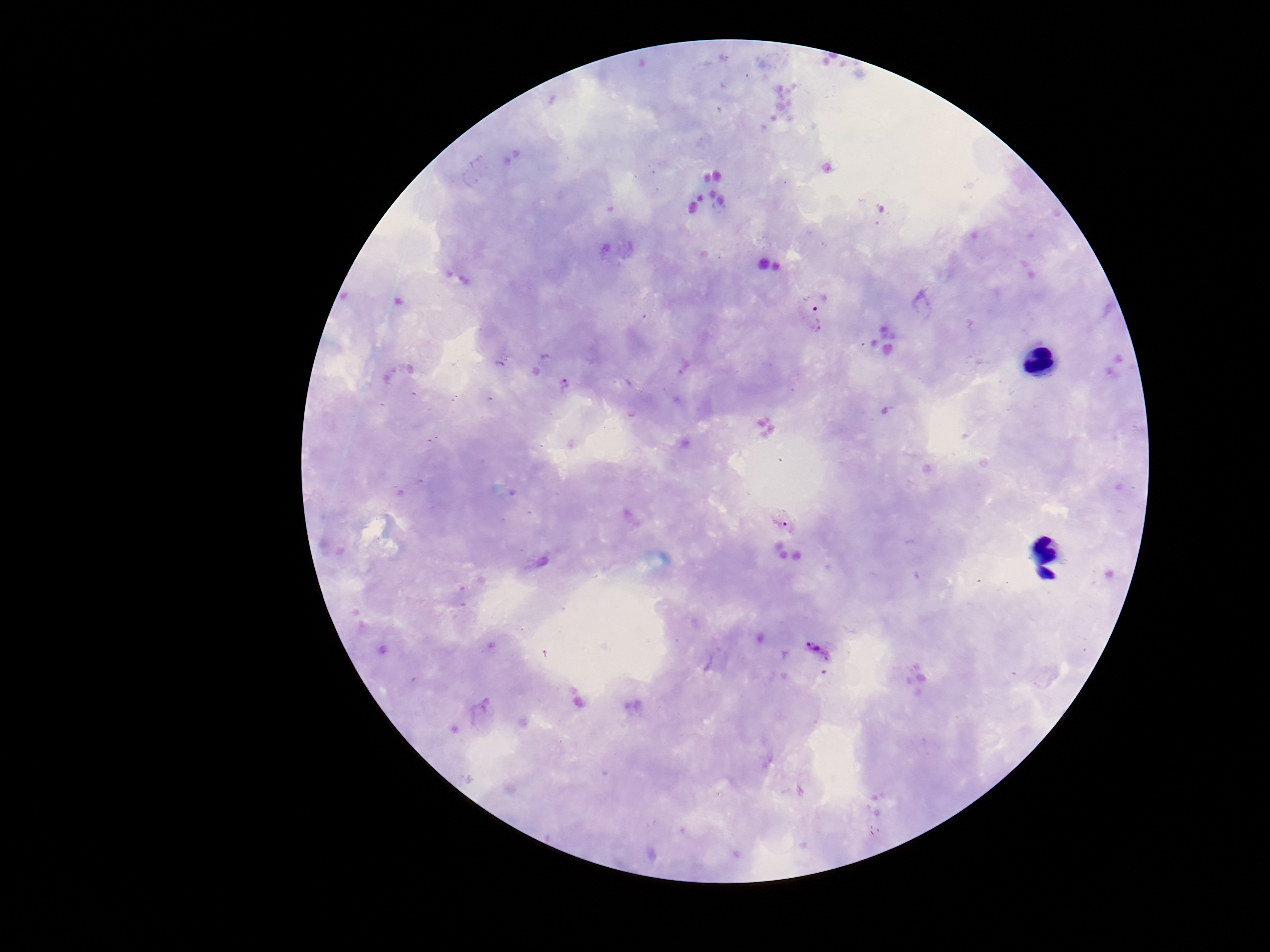
Approximate object centers, in pixels from the top-left corner.
Summary:
  - Plasmodium parasite locations: (x=814, y=316), (x=564, y=384), (x=781, y=522), (x=818, y=651)
  - Preparation: thick blood film
  - Image size: 1270×952 pixels
  - Stain: Giemsa
  - Field of view: single
  - Patient malaria status: infected
  - Capture: smartphone camera through the microscope eyepiece
  - Magnification: 100x